Identify the parasite.
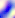
This is Toxoplasma gondii.

Captured at 400x magnification. Micrograph.